Outline each Plasmodium falciparum-infected red blood cell.
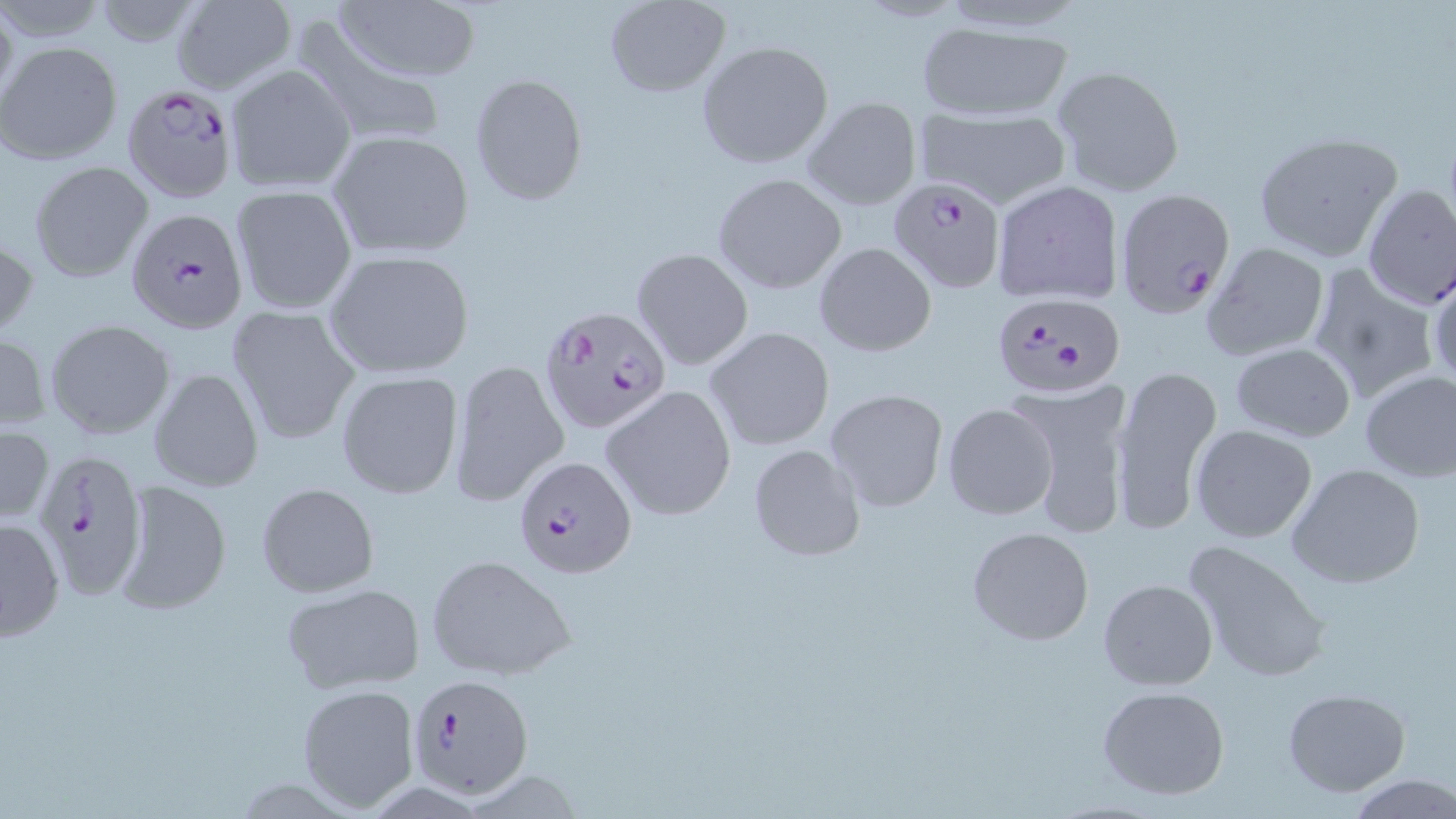
Approximate bounding boxes as (x1,y1)-(x2,y2) corner pairs in pixels.
Plasmodium falciparum-infected red blood cells (subset): (120,81)-(240,204), (888,176)-(1008,294), (127,207)-(249,335), (992,290)-(1126,400), (539,305)-(671,433), (31,449)-(148,598), (514,455)-(638,581), (404,672)-(535,798).

Summary:
  - Uninfected red blood cell locations (subset): (333,0)-(482,85), (170,1)-(298,94), (604,1)-(730,97), (293,20)-(449,148), (915,21)-(1072,121), (697,41)-(834,169), (0,42)-(122,164), (224,63)-(355,194), (1049,63)-(1184,196), (469,72)-(588,205), (801,96)-(922,211), (917,105)-(1070,207), (326,130)-(475,261), (1251,133)-(1405,263), (29,161)-(153,282), (713,173)-(847,294), (991,178)-(1125,306), (1360,183)-(1455,311), (229,184)-(357,315), (0,231)-(36,341), (813,241)-(936,355), (1199,241)-(1330,363), (632,247)-(752,370), (323,250)-(477,380), (1427,265)-(1456,393), (1305,266)-(1441,405), (226,305)-(360,445), (46,318)-(175,439), (705,325)-(834,450), (0,332)-(51,431), (1230,342)-(1356,442), (448,359)-(570,507), (1110,360)-(1223,533), (149,367)-(264,493), (1358,368)-(1456,483), (336,371)-(464,500), (1014,382)-(1132,539), (599,385)-(737,521), (825,388)-(949,512), (943,401)-(1058,521), (1189,423)-(1317,543), (0,424)-(51,524), (749,444)-(865,561), (1285,463)-(1427,590), (115,478)-(232,614), (256,482)-(380,598), (1,517)-(65,642), (967,527)-(1094,645), (1182,540)-(1330,684), (425,553)-(578,680), (1098,578)-(1218,691), (280,581)-(427,692), (296,683)-(420,811), (1097,685)-(1230,800), (1281,687)-(1412,796), (1350,775)-(1456,817)
  - Slide-level diagnosis: Plasmodium falciparum
  - Modality: light microscopy
  - Magnification: 1000x
  - Image size: 1456×819 pixels
  - Stain: May-Grünwald-Giemsa
  - Preparation: thin blood film
  - Field of view: one of a larger specimen